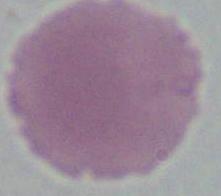
Captured at 1000x magnification. An erythrocyte is seen. Photomicrograph.